Give the position of every leukocyte visible.
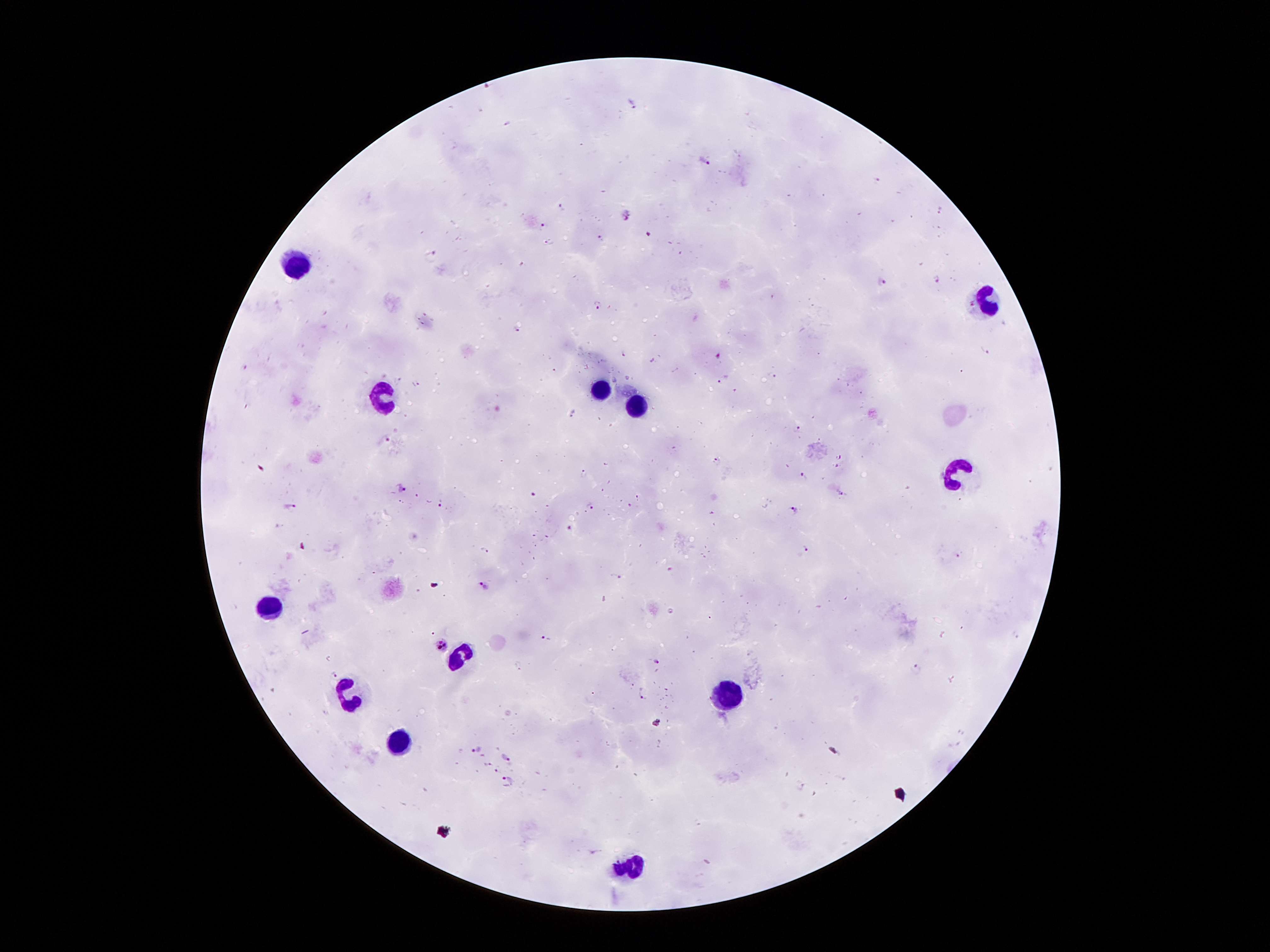

Approximate centers as (x, y) in pixels.
Leukocytes: (297, 266), (984, 302), (601, 389), (383, 398), (638, 407), (959, 471), (269, 608), (457, 656), (734, 693), (358, 698), (403, 742), (630, 865).

Plasmodium parasite locations: (488, 87), (634, 103), (507, 121), (704, 163), (876, 179), (562, 207), (940, 210), (626, 215), (543, 226), (648, 233), (602, 237), (548, 242), (433, 254), (522, 263), (936, 281), (882, 283), (597, 305), (516, 330), (984, 350), (623, 353), (718, 355), (244, 366), (772, 374), (723, 379), (399, 380), (417, 383), (574, 414), (799, 430), (388, 440), (839, 455), (718, 462), (838, 466), (585, 474), (805, 476), (401, 488), (842, 494), (533, 496), (442, 503), (631, 505), (289, 506), (591, 507), (793, 508), (569, 529), (805, 549), (485, 551), (958, 555), (671, 569), (616, 576), (483, 586), (546, 639), (441, 644), (657, 661), (917, 667), (335, 674), (643, 695), (475, 748), (506, 758), (487, 763), (496, 770), (507, 780). 100x magnification. Smartphone photograph taken through the microscope eyepiece. Patient malaria status: infected with Plasmodium falciparum. Giemsa-stained preparation. One field from this slide. Image is 1270×952 pixels. Thick blood film.